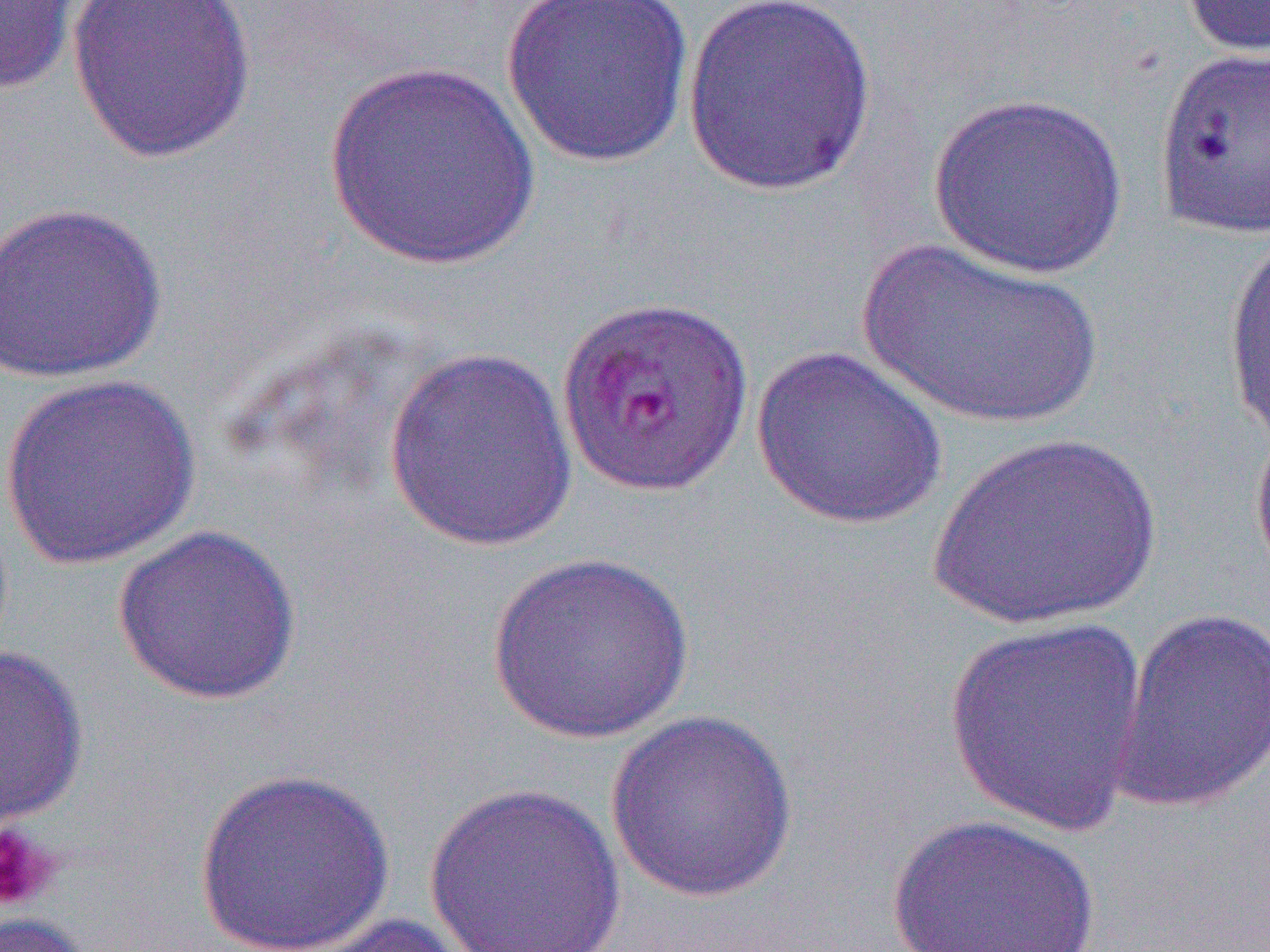

Approximate bounding boxes as named x1/y1/x2/y2 corners in pixels. Platelet locations: (x1=0, y1=821, x2=60, y2=913). Uninfected red blood cell locations: (x1=66, y1=0, x2=259, y2=165), (x1=499, y1=0, x2=697, y2=170), (x1=1178, y1=0, x2=1270, y2=59), (x1=0, y1=1, x2=83, y2=97), (x1=680, y1=1, x2=878, y2=198), (x1=1152, y1=45, x2=1270, y2=241), (x1=320, y1=60, x2=543, y2=272), (x1=928, y1=91, x2=1128, y2=278), (x1=0, y1=200, x2=168, y2=384), (x1=1221, y1=228, x2=1270, y2=453), (x1=857, y1=236, x2=1104, y2=430), (x1=751, y1=345, x2=947, y2=530), (x1=383, y1=347, x2=580, y2=553), (x1=1, y1=372, x2=203, y2=570), (x1=925, y1=433, x2=1165, y2=631), (x1=111, y1=524, x2=303, y2=706), (x1=486, y1=551, x2=694, y2=744), (x1=1107, y1=606, x2=1270, y2=815), (x1=943, y1=613, x2=1150, y2=834), (x1=0, y1=644, x2=89, y2=831), (x1=605, y1=709, x2=800, y2=902), (x1=194, y1=768, x2=395, y2=951), (x1=423, y1=781, x2=626, y2=952), (x1=885, y1=813, x2=1103, y2=952), (x1=0, y1=912, x2=95, y2=952), (x1=288, y1=912, x2=479, y2=952). Slide-level diagnosis: Plasmodium falciparum. Light microscopy. Thin blood film. Image is 1270×952 pixels. 1000x magnification. Single field of view.